Outline each blood parasite and name the species.
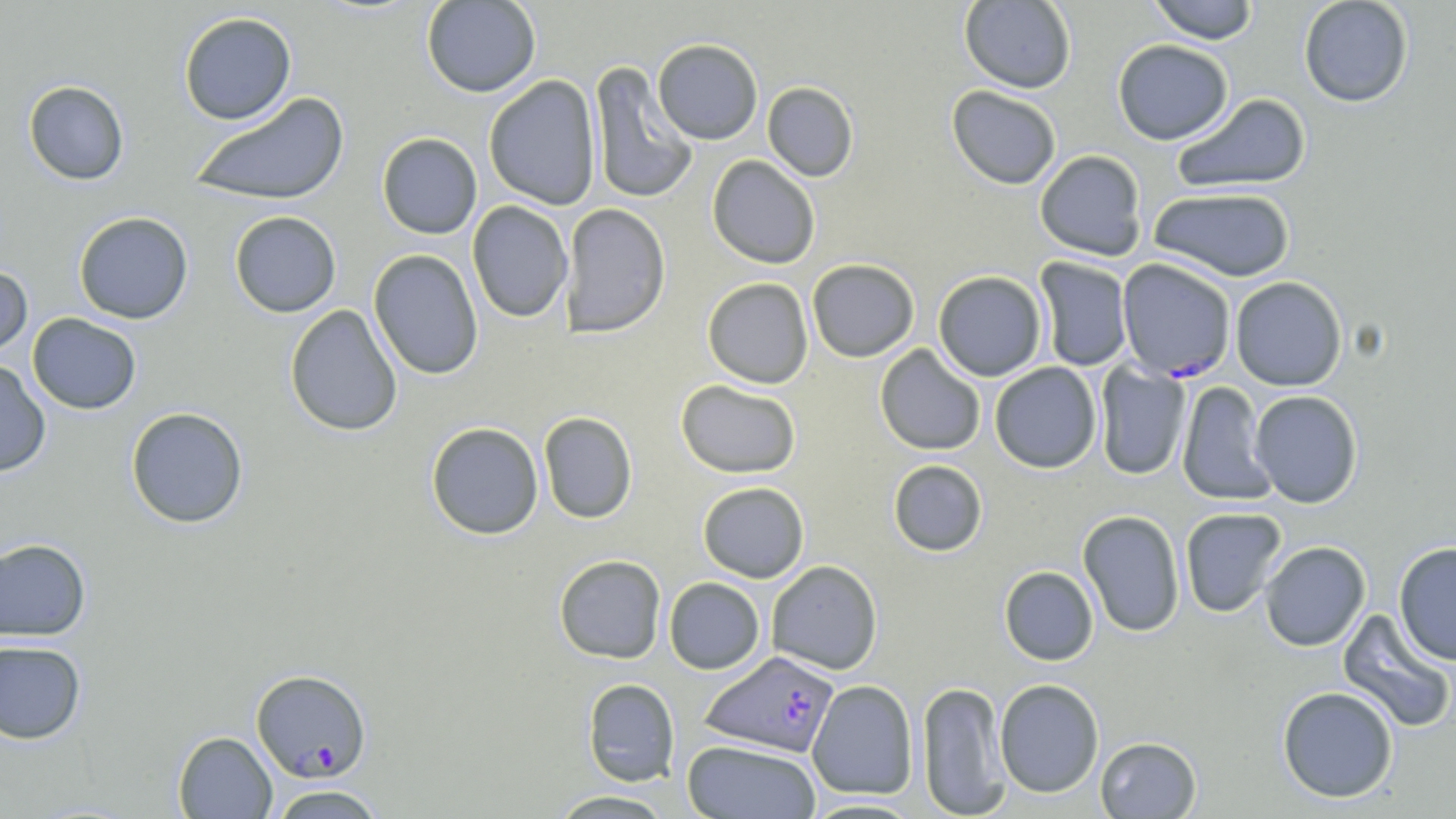
Approximate bounding boxes as (x1, y1, x2, y2) in pixels.
Plasmodium falciparum-infected red blood cells: (1116, 258, 1236, 382), (699, 651, 839, 757), (251, 669, 372, 782).
No Plasmodium ovale, Plasmodium malariae, Plasmodium vivax, Babesia divergens, or Trypanosoma brucei observed.

slide_level_diagnosis: Plasmodium falciparum
stain: May-Grünwald-Giemsa
preparation: thin blood smear
field_of_view: one of a larger specimen
modality: optical microscopy
magnification: 1000x
uninfected_red_blood_cell_locations: 'approximate bounding boxes as (x1, y1, x2, y2) in pixels: (421, 0, 541, 97), (959, 0, 1076, 93), (1147, 0, 1260, 44), (1298, 0, 1414, 108), (178, 11, 297, 125), (652, 38, 763, 145), (1112, 39, 1234, 145), (588, 60, 698, 205), (483, 76, 602, 210), (22, 80, 130, 186), (762, 82, 859, 182), (946, 85, 1062, 189), (188, 91, 350, 208), (1171, 93, 1312, 194), (377, 132, 482, 239), (1034, 149, 1148, 261), (707, 155, 821, 269), (1148, 186, 1296, 282), (467, 201, 573, 323), (560, 203, 671, 338), (73, 211, 193, 324), (229, 211, 341, 318), (369, 249, 483, 380), (1034, 257, 1134, 372), (806, 258, 920, 362), (0, 264, 33, 361), (932, 270, 1047, 381), (1230, 276, 1347, 391), (702, 277, 813, 389), (284, 304, 403, 436), (27, 313, 142, 414), (874, 344, 986, 456), (0, 359, 51, 477), (1094, 361, 1191, 480), (989, 362, 1102, 473), (675, 379, 801, 479), (1177, 380, 1276, 505), (1248, 390, 1363, 508), (125, 407, 249, 529), (538, 411, 638, 524), (426, 422, 544, 540), (888, 459, 988, 556), (697, 481, 809, 583), (1180, 507, 1287, 618), (1077, 509, 1186, 637), (0, 538, 92, 642), (1259, 541, 1371, 651), (1393, 541, 1456, 665), (553, 554, 667, 664), (766, 560, 883, 675), (999, 566, 1099, 666), (663, 577, 765, 675), (1337, 609, 1456, 733), (0, 640, 86, 744), (582, 678, 680, 786), (994, 678, 1104, 798), (807, 679, 919, 799), (916, 680, 1009, 818), (1276, 685, 1399, 803), (172, 731, 277, 818), (1095, 736, 1202, 818), (681, 740, 821, 818), (267, 784, 387, 818), (546, 789, 678, 818), (800, 797, 924, 818)'
image_size: 1456×819 pixels